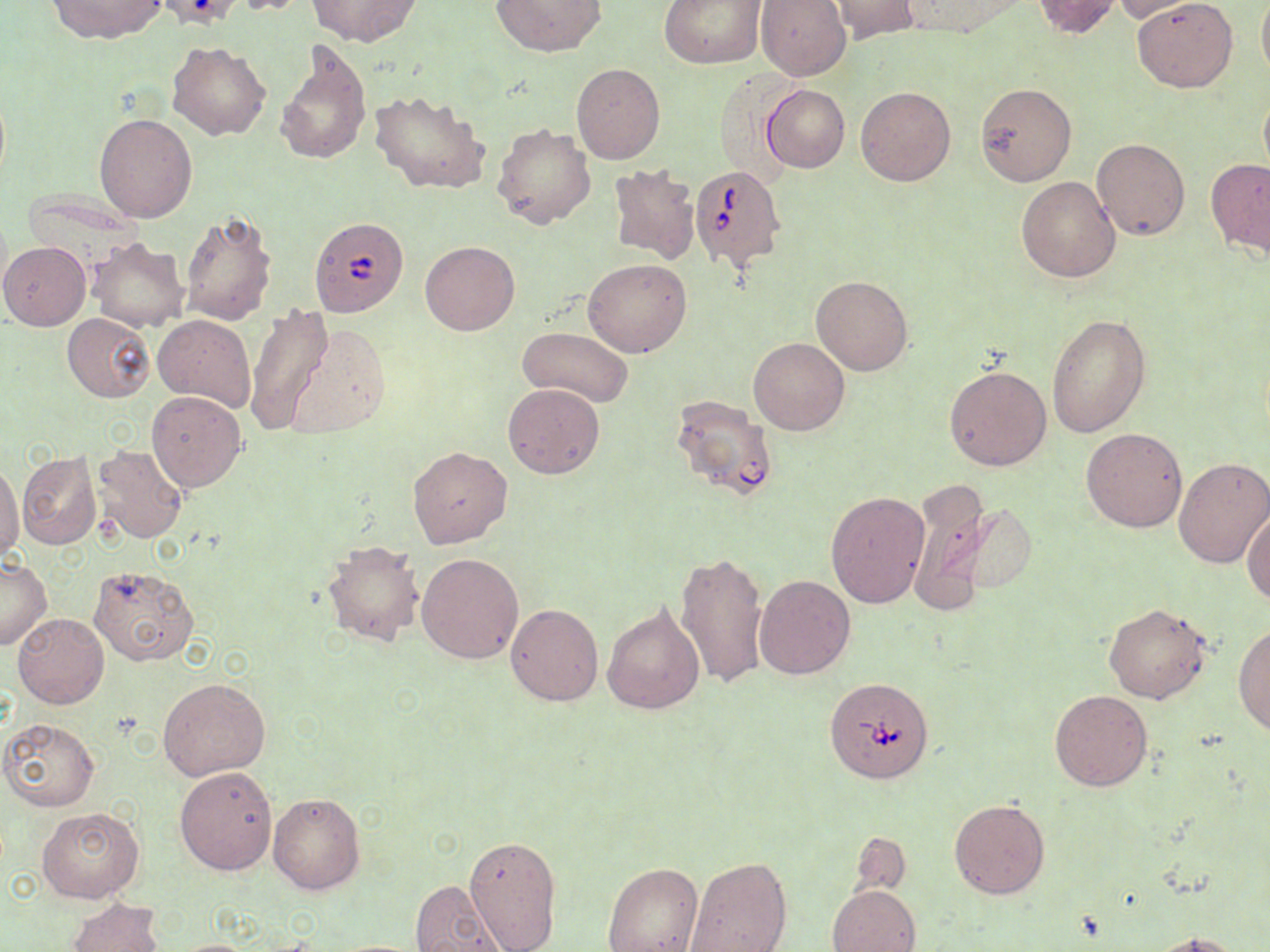
{
  "slide_level_diagnosis": "Babesia divergens",
  "uninfected_red_blood_cell_locations": "approximate bounding boxes as named x1/y1/x2/y2 corners in pixels: (x1=46, y1=0, x2=167, y2=42), (x1=227, y1=0, x2=314, y2=15), (x1=306, y1=0, x2=421, y2=47), (x1=491, y1=0, x2=606, y2=56), (x1=661, y1=0, x2=768, y2=68), (x1=756, y1=0, x2=850, y2=81), (x1=830, y1=0, x2=921, y2=43), (x1=897, y1=0, x2=1029, y2=38), (x1=1032, y1=0, x2=1122, y2=39), (x1=1132, y1=0, x2=1237, y2=91), (x1=1257, y1=0, x2=1270, y2=83), (x1=1112, y1=1, x2=1201, y2=22), (x1=275, y1=39, x2=371, y2=166), (x1=167, y1=42, x2=271, y2=141), (x1=571, y1=63, x2=665, y2=164), (x1=975, y1=82, x2=1077, y2=185), (x1=0, y1=85, x2=10, y2=191), (x1=762, y1=85, x2=849, y2=172), (x1=856, y1=86, x2=956, y2=187), (x1=370, y1=88, x2=492, y2=195), (x1=1258, y1=91, x2=1270, y2=181), (x1=94, y1=113, x2=199, y2=222), (x1=492, y1=124, x2=596, y2=230), (x1=1092, y1=138, x2=1191, y2=240), (x1=1207, y1=158, x2=1270, y2=257), (x1=607, y1=165, x2=701, y2=264), (x1=1016, y1=175, x2=1120, y2=281), (x1=179, y1=211, x2=277, y2=325), (x1=86, y1=236, x2=190, y2=331), (x1=421, y1=241, x2=520, y2=336), (x1=1, y1=242, x2=90, y2=330), (x1=584, y1=258, x2=691, y2=358), (x1=810, y1=275, x2=913, y2=376), (x1=244, y1=307, x2=334, y2=434), (x1=62, y1=312, x2=154, y2=402), (x1=1048, y1=312, x2=1151, y2=437), (x1=154, y1=314, x2=256, y2=411), (x1=289, y1=324, x2=391, y2=443), (x1=519, y1=326, x2=634, y2=408), (x1=749, y1=336, x2=850, y2=435), (x1=944, y1=363, x2=1053, y2=472), (x1=504, y1=383, x2=605, y2=479), (x1=147, y1=390, x2=247, y2=491), (x1=1082, y1=428, x2=1188, y2=533), (x1=90, y1=444, x2=188, y2=544), (x1=407, y1=446, x2=512, y2=549), (x1=17, y1=451, x2=100, y2=550), (x1=1173, y1=456, x2=1270, y2=569), (x1=0, y1=461, x2=24, y2=564), (x1=911, y1=488, x2=1038, y2=611), (x1=826, y1=491, x2=930, y2=609), (x1=1244, y1=507, x2=1270, y2=606), (x1=321, y1=538, x2=426, y2=648), (x1=417, y1=552, x2=525, y2=664), (x1=675, y1=553, x2=770, y2=689), (x1=1, y1=557, x2=51, y2=651), (x1=89, y1=563, x2=199, y2=667), (x1=754, y1=575, x2=855, y2=679), (x1=1103, y1=602, x2=1213, y2=704), (x1=505, y1=603, x2=603, y2=706), (x1=602, y1=603, x2=706, y2=715), (x1=11, y1=612, x2=108, y2=710), (x1=1233, y1=622, x2=1270, y2=737), (x1=158, y1=676, x2=271, y2=780), (x1=1049, y1=689, x2=1153, y2=791), (x1=1, y1=717, x2=100, y2=812), (x1=175, y1=764, x2=279, y2=875), (x1=267, y1=793, x2=365, y2=895), (x1=948, y1=800, x2=1050, y2=900), (x1=36, y1=806, x2=144, y2=903), (x1=853, y1=831, x2=909, y2=892), (x1=464, y1=834, x2=562, y2=952), (x1=683, y1=855, x2=792, y2=952), (x1=602, y1=861, x2=704, y2=952), (x1=408, y1=880, x2=508, y2=952), (x1=828, y1=883, x2=920, y2=952), (x1=67, y1=898, x2=165, y2=952), (x1=1151, y1=931, x2=1243, y2=952)",
  "babesia_divergens_infected_red_blood_cell_locations": "approximate bounding boxes as named x1/y1/x2/y2 corners in pixels: (x1=689, y1=164, x2=787, y2=271), (x1=311, y1=218, x2=406, y2=319), (x1=676, y1=399, x2=775, y2=501), (x1=825, y1=676, x2=935, y2=783)",
  "preparation": "thin blood film",
  "field_of_view": "one of a larger specimen",
  "stain": "May-Grünwald-Giemsa",
  "image_size": "1270×952 pixels",
  "magnification": "1000x",
  "modality": "optical microscopy"
}